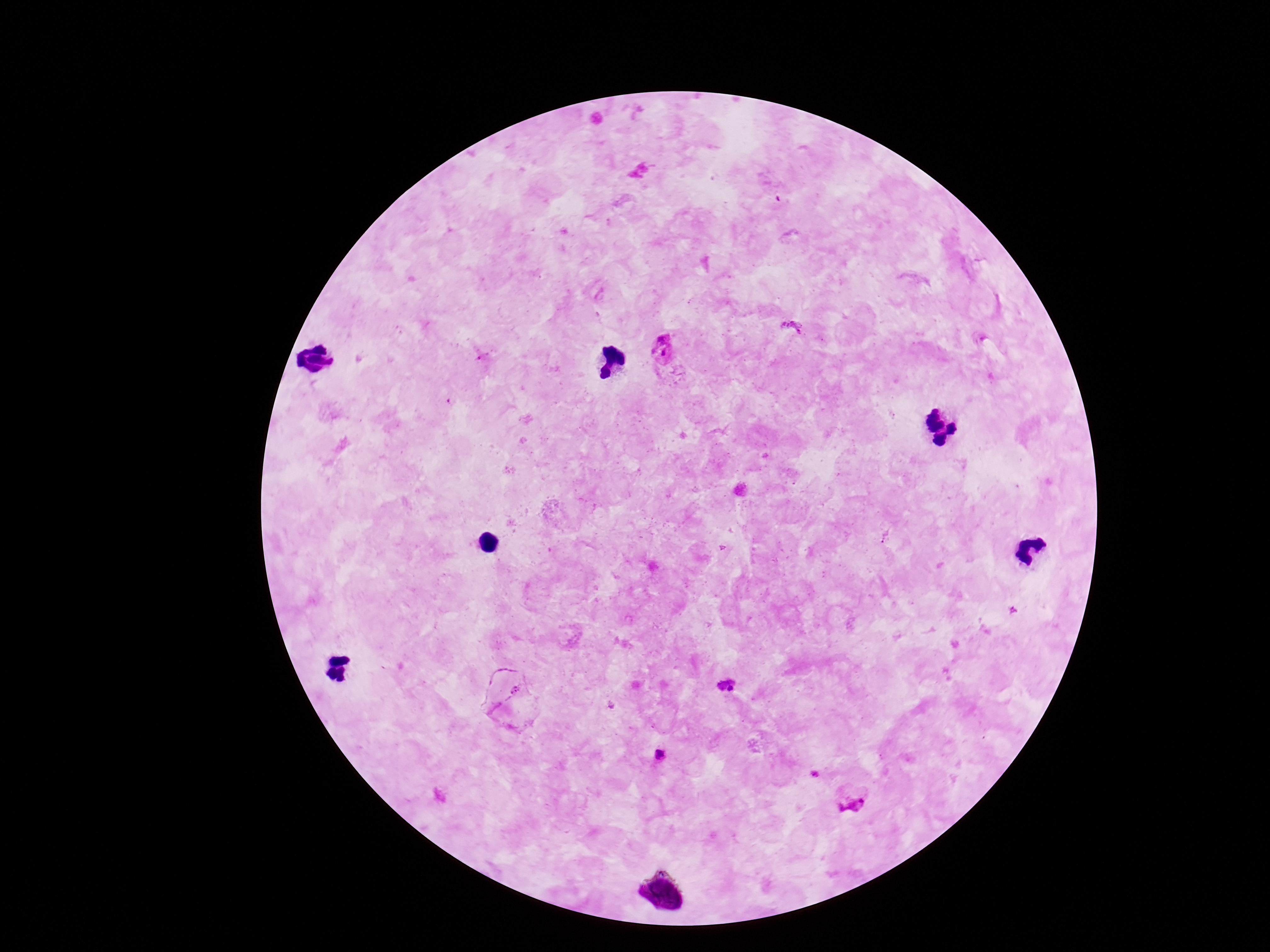
Approximate centers as [x, y] in pixels. Plasmodium parasite locations: [792, 330], [662, 352], [885, 535], [726, 684], [516, 691], [661, 755], [814, 774], [852, 798]. Smartphone photograph taken through the microscope eyepiece. 100x magnification. Giemsa-stained preparation. Single field of view. Image is 1270×952 pixels. Thick blood film. Patient malaria status: positive.